Point out each Plasmodium parasite.
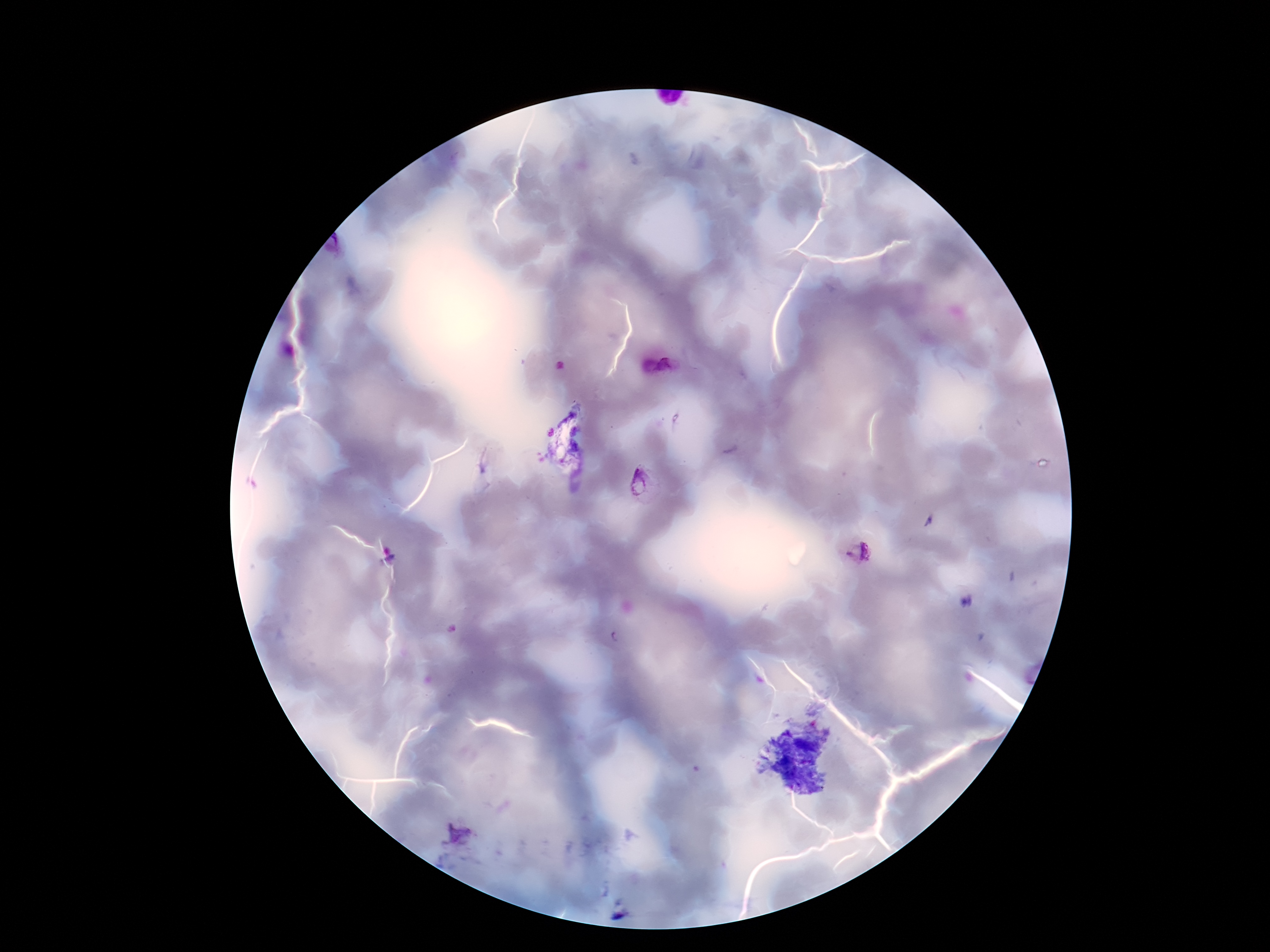
Approximate object centers, in pixels from the top-left corner.
Plasmodium parasites: (x=657, y=366), (x=646, y=486), (x=857, y=552), (x=458, y=835).

One field from this slide. Thick blood film. Smartphone photograph taken through the microscope eyepiece. Patient malaria status: positive. Giemsa stain. Image is 1270×952 pixels. 100x magnification.